Give the position of every Plasmodium parasite, noting whether each is a trophozoite, schizont, or gametocyte.
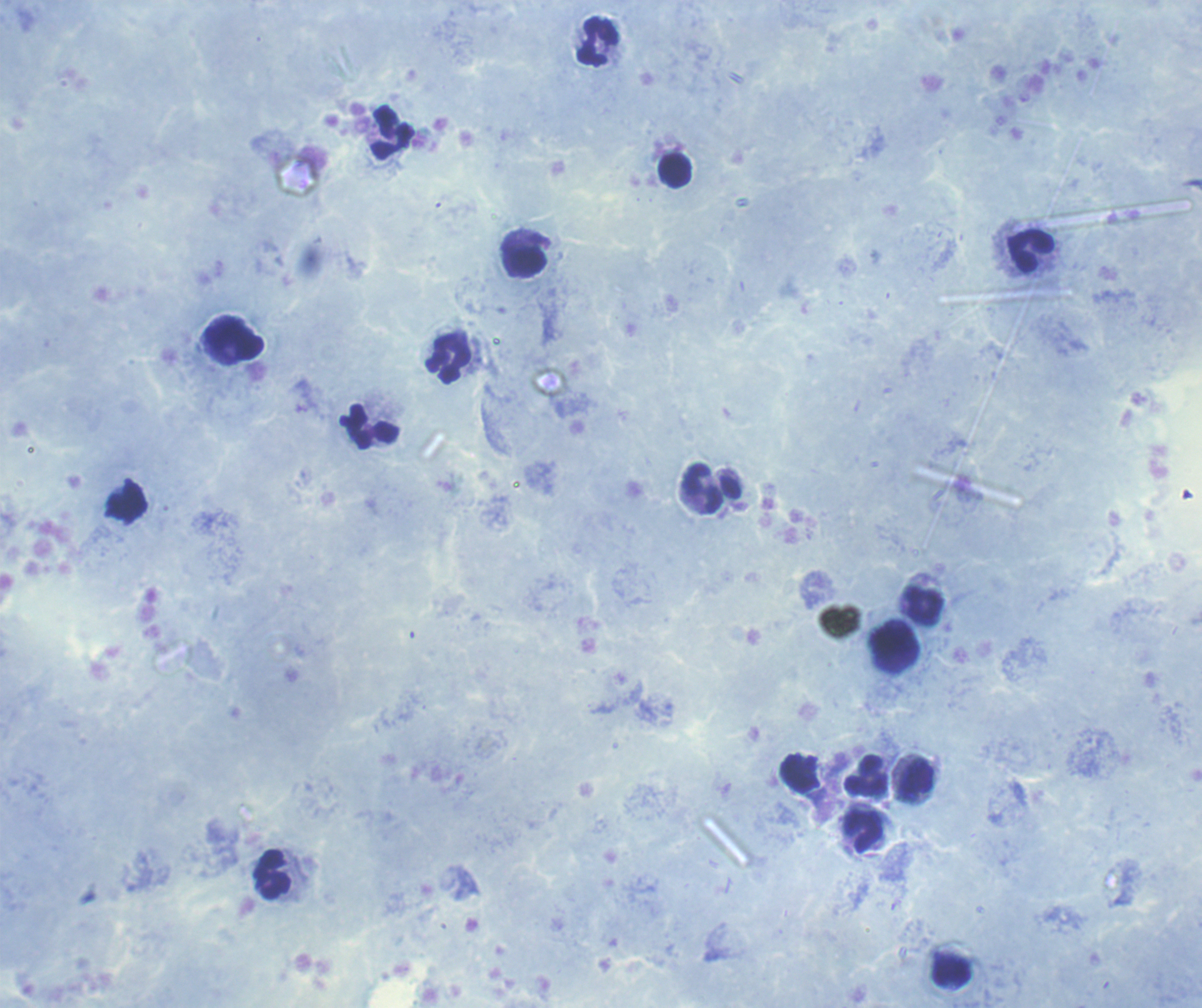

No Plasmodium parasites detected.

{
  "leukocyte_locations": "approximate centers as {x, y} in pixels: {598, 42}, {394, 133}, {675, 171}, {1030, 251}, {526, 263}, {234, 341}, {449, 358}, {370, 427}, {702, 488}, {923, 604}, {895, 641}, {867, 775}, {917, 780}, {864, 830}, {273, 874}",
  "stain": "Romanowsky",
  "preparation": "thick smear of blood",
  "magnification": "100x",
  "background_quality": "good",
  "image_size": "1202×1008 pixels",
  "context": "previously used in a real diagnosis",
  "field_of_view": "one from this slide",
  "coloration_quality": "good"
}